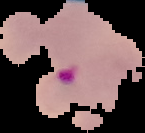
preparation = thin blood film
image type = cell region segmented out of the field of view; surrounding area masked to black
image size = 145×133 pixels
result = malaria parasites detected